Identify the preparation type.
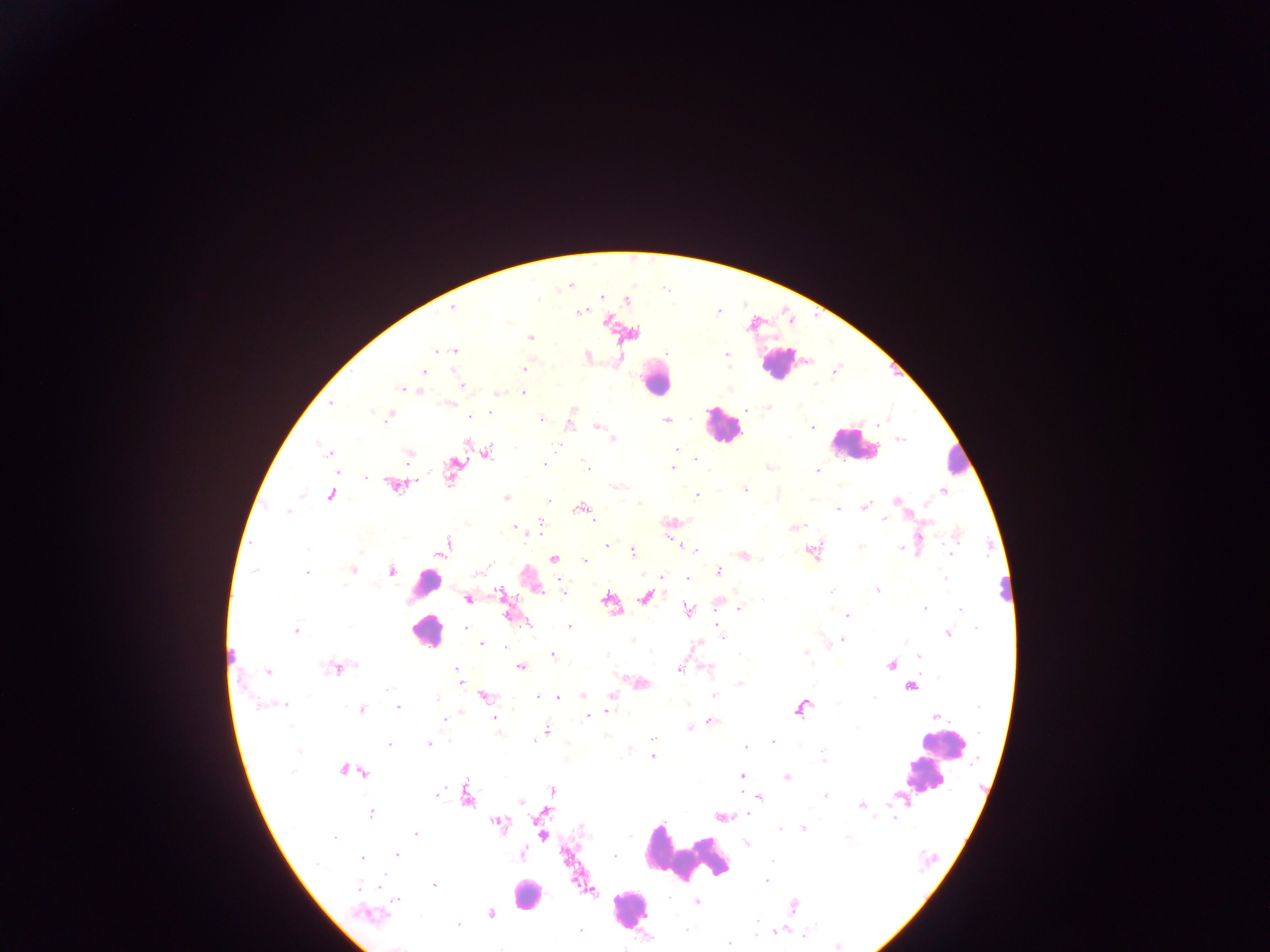

This is a thick smear.

leukocyte locations = approximate centers as {x, y} in pixels: {780, 363}, {655, 379}, {723, 425}, {854, 445}, {952, 464}, {421, 585}, {1007, 589}, {427, 630}, {230, 658}, {939, 748}, {924, 776}, {687, 856}, {526, 894}, {630, 909}
country = Ghana
capture = mobile-phone photograph through a microscope
image size = 1270×952 pixels
Plasmodium parasite locations = approximate centers as {x, y} in pixels: {570, 285}, {601, 296}, {538, 299}, {627, 300}, {452, 307}, {580, 313}, {530, 337}, {436, 350}, {455, 350}, {667, 353}, {725, 353}, {588, 356}, {524, 369}, {423, 371}, {462, 386}, {402, 389}, {410, 390}, {418, 391}, {523, 393}, {496, 394}, {331, 403}, {449, 404}, {768, 407}, {745, 409}, {573, 410}, {372, 412}, {490, 413}, {389, 417}, {470, 417}, {542, 419}, {666, 420}, {570, 424}, {597, 426}, {812, 427}, {614, 439}, {901, 439}, {466, 445}, {557, 446}, {678, 449}, {330, 452}, {488, 452}, {408, 455}, {695, 458}, {544, 465}, {769, 466}, {587, 467}, {673, 468}, {818, 471}, {452, 472}, {366, 477}, {394, 486}, {613, 486}, {745, 490}, {943, 491}, {696, 495}, {331, 496}, {506, 498}, {549, 500}, {896, 501}, {928, 503}, {865, 507}, {581, 508}, {837, 509}, {287, 512}, {883, 519}, {593, 520}, {541, 521}, {514, 526}, {794, 528}, {956, 534}, {607, 546}, {444, 547}, {861, 547}, {900, 548}, {695, 549}, {811, 551}, {359, 552}, {633, 552}, {951, 552}, {742, 555}, {553, 558}, {584, 561}, {255, 570}, {352, 570}, {719, 570}, {391, 571}, {480, 571}, {307, 572}, {663, 576}, {687, 577}, {945, 578}, {877, 590}, {831, 591}, {563, 592}, {500, 593}, {646, 597}, {468, 599}, {609, 601}, {739, 608}, {924, 608}, {688, 609}, {960, 609}, {847, 616}, {508, 617}, {718, 623}, {570, 627}, {466, 628}, {976, 628}, {295, 631}, {948, 634}, {723, 637}, {632, 640}, {843, 640}, {481, 643}, {697, 645}, {831, 645}, {504, 647}, {805, 652}, {552, 656}, {918, 657}, {891, 665}, {521, 667}, {335, 668}, {679, 669}, {456, 670}, {709, 670}, {268, 672}, {459, 676}, {939, 678}, {461, 681}, {642, 683}, {740, 683}, {911, 687}, {389, 689}, {714, 695}, {485, 696}, {583, 696}, {611, 696}, {537, 697}, {438, 698}, {559, 698}, {874, 698}, {285, 704}, {837, 704}, {688, 705}, {259, 706}, {978, 706}, {398, 708}, {361, 709}, {800, 709}, {609, 711}, {588, 717}, {936, 717}, {494, 718}, {444, 719}, {711, 721}, {290, 727}, {856, 728}, {689, 729}, {545, 731}, {538, 736}, {652, 739}, {534, 740}, {772, 742}, {389, 744}, {429, 744}, {800, 745}, {746, 747}, {652, 750}, {299, 752}, {652, 756}, {824, 759}, {345, 769}, {361, 770}, {292, 772}, {742, 776}, {786, 777}, {552, 790}, {438, 794}, {467, 796}, {826, 796}, {759, 798}, {520, 802}, {861, 806}, {371, 813}, {747, 814}, {722, 818}, {894, 819}, {499, 824}, {581, 829}, {781, 829}, {803, 829}, {415, 834}, {542, 835}, {335, 838}, {747, 844}, {522, 854}, {397, 855}, {614, 857}, {362, 858}, {773, 862}, {317, 864}, {766, 881}, {435, 886}, {360, 888}, {668, 897}, {396, 902}, {696, 902}, {793, 906}, {491, 914}, {366, 915}, {756, 921}, {458, 925}, {580, 930}, {686, 930}, {777, 930}, {757, 933}, {805, 936}, {728, 944}, {837, 946}
field of view = single